Assess this cell for malaria.
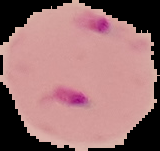

Parasitized.

{
  "preparation": "thin blood film",
  "image_type": "cell region segmented out of the field of view; surrounding area masked to black",
  "image_size": "160×151 pixels"
}